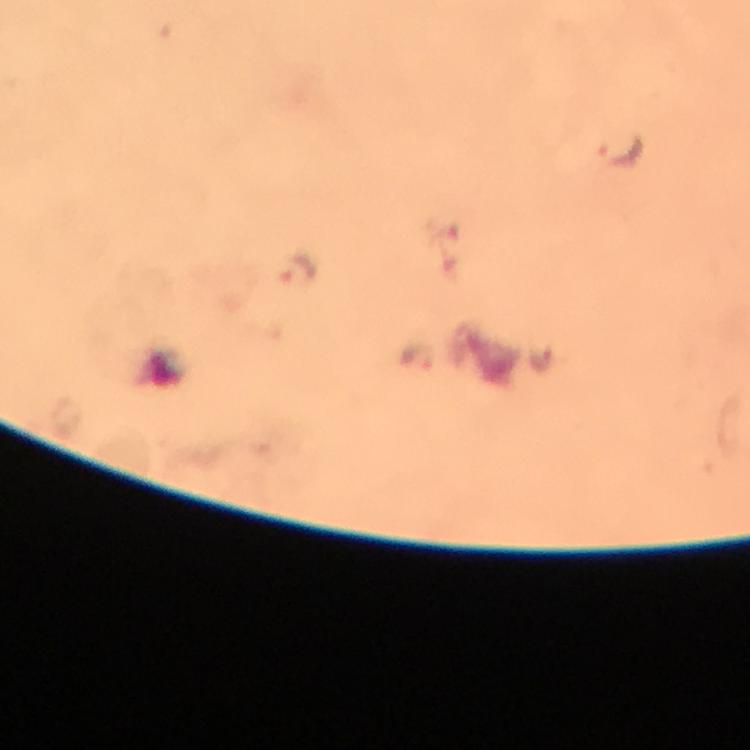

capture = smartphone photograph through a microscope
Plasmodium parasite locations = approximate centers as (x, y) in pixels: (622, 154), (302, 269), (417, 354), (543, 361)
preparation = thick blood film
magnification = 100x
stain = Giemsa
context = from a diagnostic examination for malaria
image size = 750×750 pixels
immersion oil = used
cropped from = a single field of view